Comment on the morphology of the red blood cells.
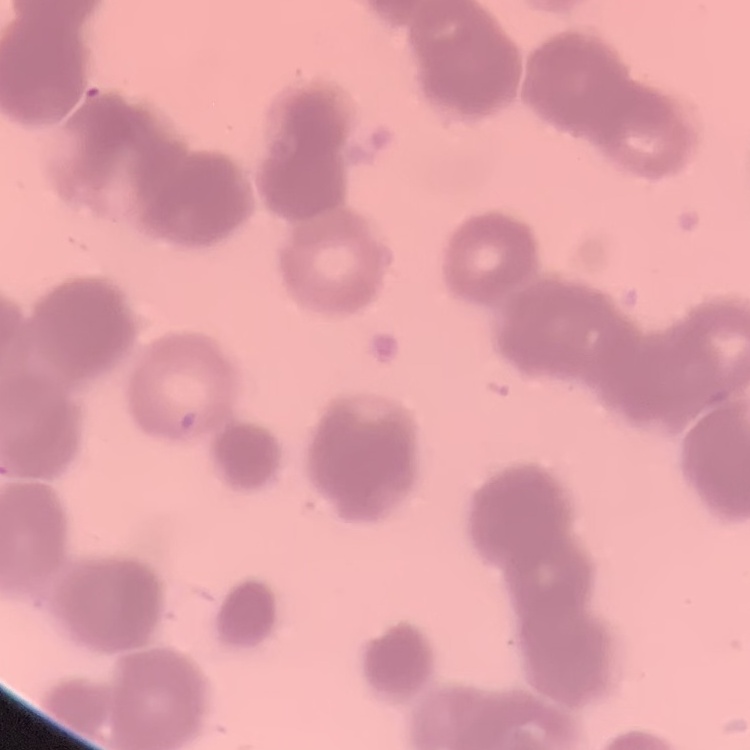
They show rouleaux formation.

stain = Field's or Giemsa
image type = one tile cut from a larger photomicrograph
preparation = thin blood smear